Assess for malaria.
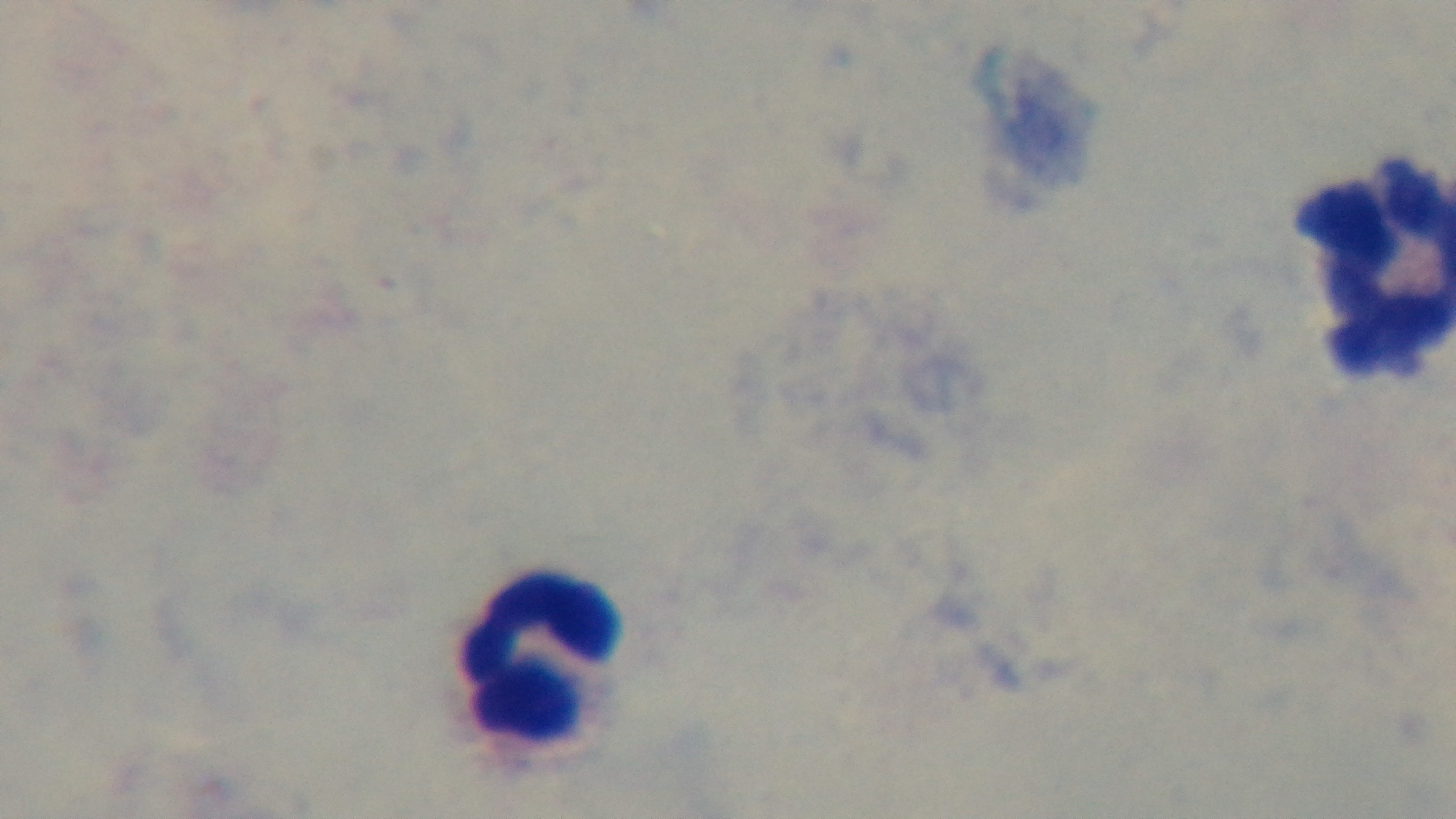

It is uninfected.

{
  "capture": "mounted 4K digital camera",
  "modality": "light microscopy",
  "stain": "Giemsa",
  "preparation": "thick",
  "objective": "100x oil immersion",
  "field_of_view": "single"
}